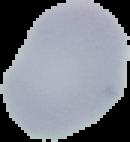

Summary:
  - Malaria status: uninfected
  - Image type: segmented cell region on a black background
  - Image size: 130×142 pixels
  - Preparation: thin blood film